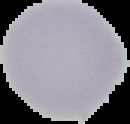

preparation = thin blood smear
result = no malaria parasites seen
image type = cell region segmented out of the field of view; surrounding area masked to black
image size = 130×124 pixels